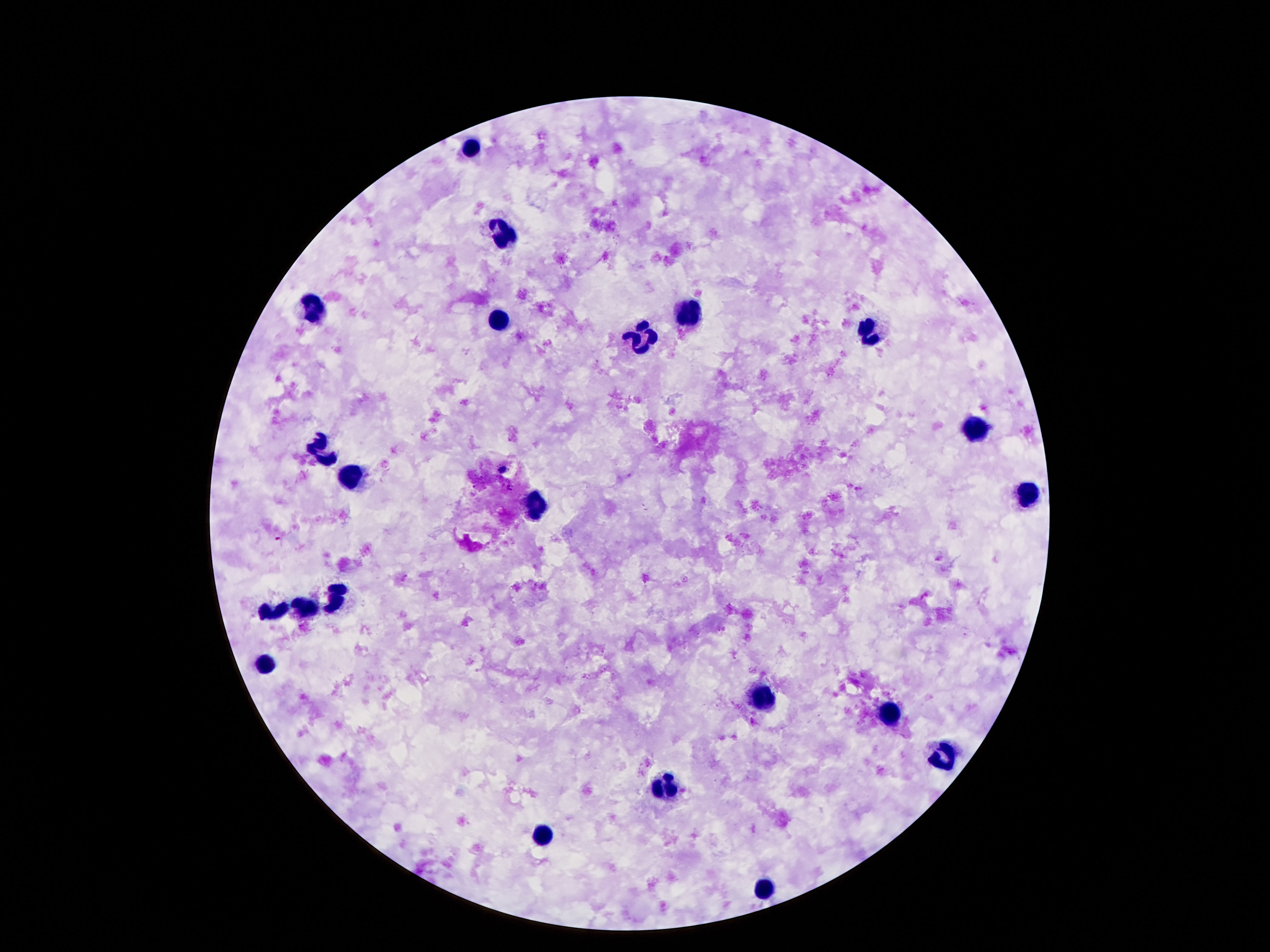
patient malaria status = uninfected
capture = smartphone camera through the microscope eyepiece
stain = Giemsa
field of view = single
leukocyte locations = approximate object centers, in pixels from the top-left corner: (x=471, y=147), (x=504, y=234), (x=318, y=306), (x=686, y=309), (x=496, y=321), (x=871, y=334), (x=645, y=341), (x=975, y=431), (x=318, y=453), (x=356, y=478), (x=1026, y=496), (x=537, y=504), (x=338, y=592), (x=305, y=607), (x=275, y=611), (x=266, y=665), (x=760, y=697), (x=893, y=717), (x=947, y=751), (x=666, y=785), (x=543, y=836), (x=764, y=887)
preparation = thick blood smear
image size = 1270×952 pixels
magnification = 100x